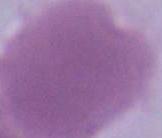

An erythrocyte is shown. Micrograph. 1000x magnification.